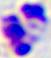
identification = leukocyte
magnification = 400x
modality = micrograph